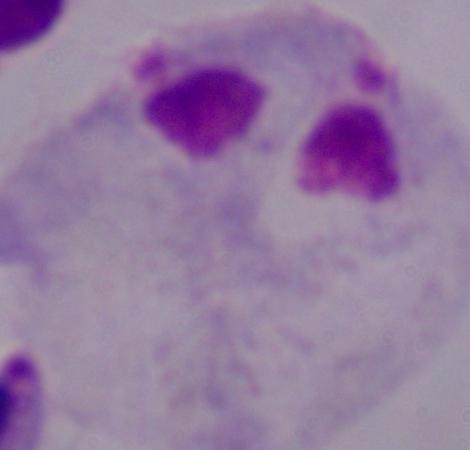
Summary:
  - Identification: trichomonad
  - Modality: micrograph
  - Magnification: 1000x